Locate every Plasmodium falciparum parasite and give its life-cycle stage, and locate every leukocyte and any debris.
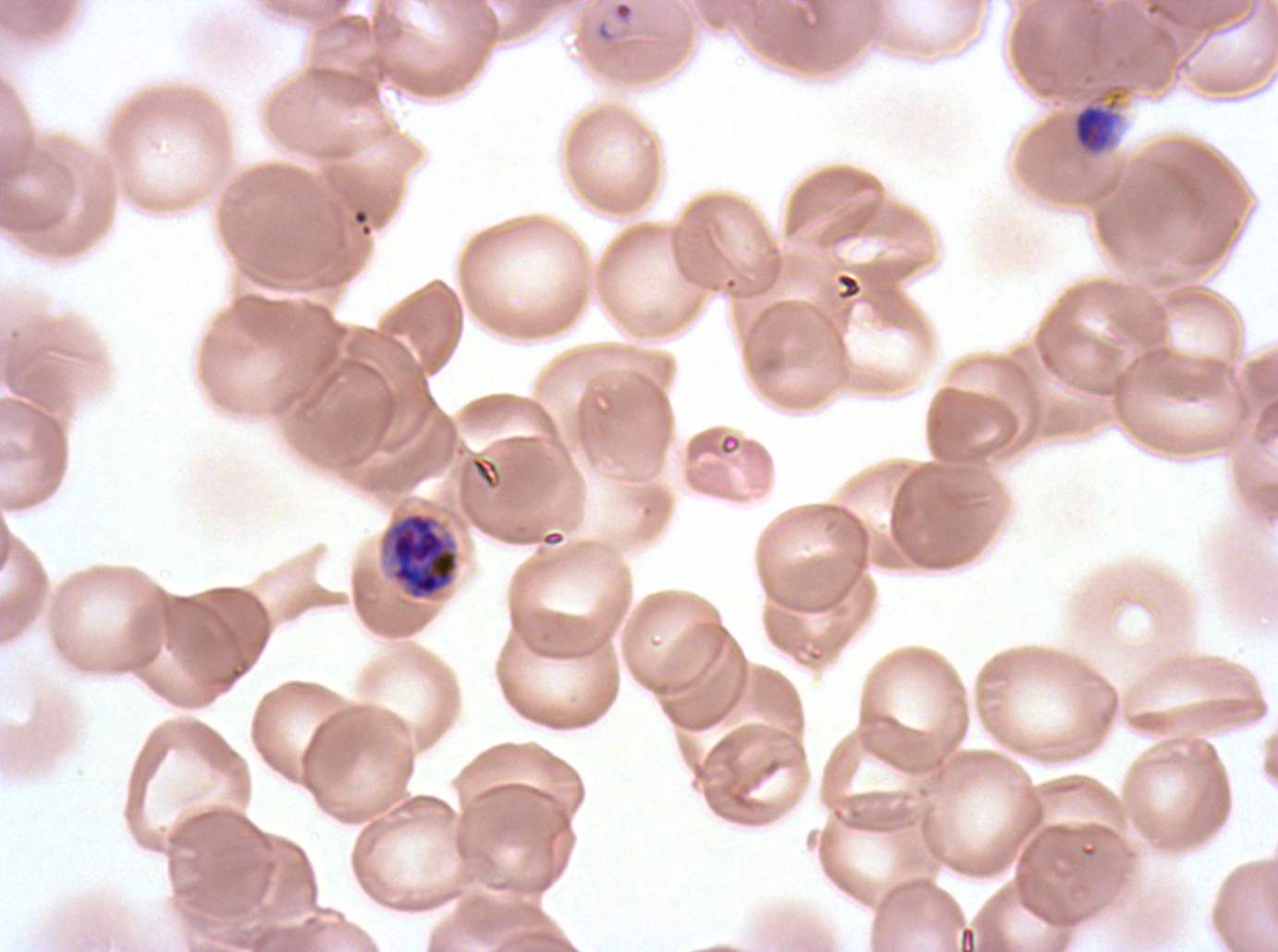

Approximate bounding boxes as [x1, y1, x2, y2] in pixels.
Rings: [611, 0, 635, 25].
Late-ring/early-trophozoite forms: [1074, 104, 1114, 152].
Early schizonts: [380, 511, 460, 601].
No mid trophozoites, late trophozoites, late schizonts, segmenters, gametocytes, leukocytes, or debris observed.

Summary:
  - Stain: Giemsa
  - Life-cycle stages observed: ring, late-ring/early-trophozoite, early schizont
  - Preparation: thin blood smear
  - Image size: 1278×952 pixels
  - Specimen: ex-vivo Plasmodium falciparum culture from a patient in The Gambia, grown for 24 to 48 hours
  - Field of view: sub-image separated from a larger composite